Assess the morphology of the erythrocytes.
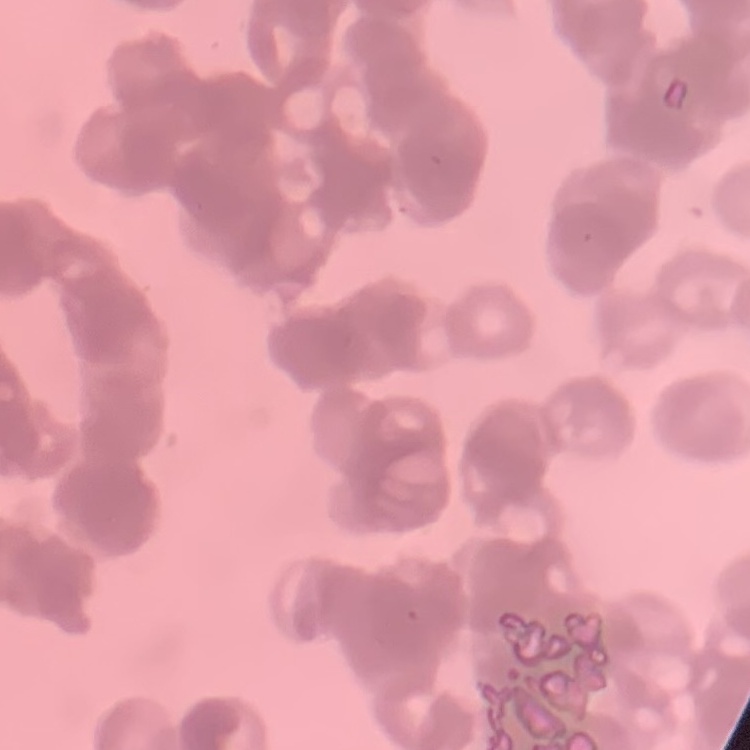

Rouleaux formation.

image type = square crop of a larger photomicrograph
stain = Field's or Giemsa
preparation = thin blood smear